Outline each uninfected red blood cell.
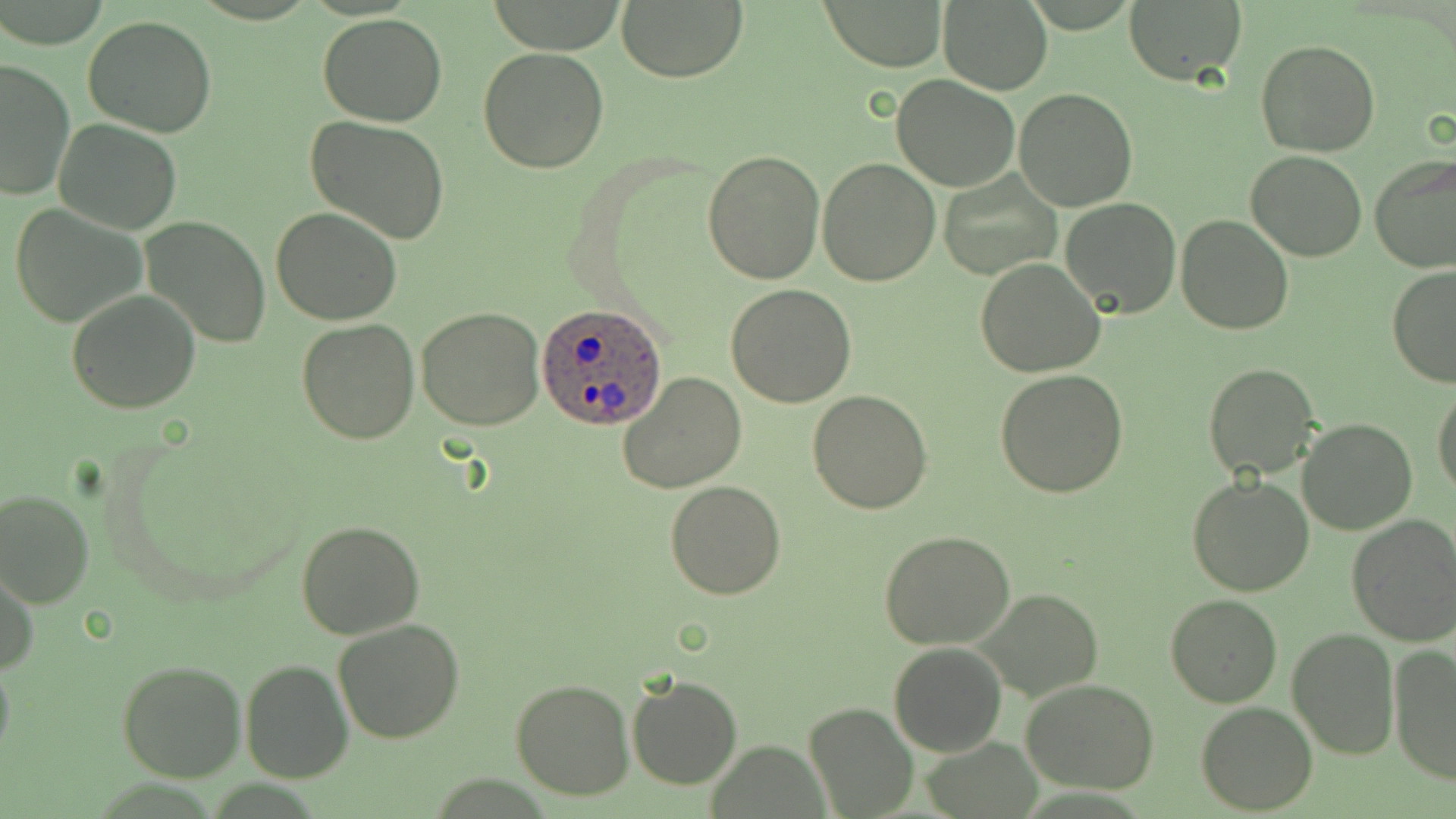
Approximate bounding boxes as (x1,y1)-(x2,y2) corner pairs in pixels.
Uninfected red blood cells: (617,0)-(746,82), (936,0)-(1054,95), (822,1)-(947,71), (1122,1)-(1247,85), (319,13)-(448,126), (82,15)-(219,138), (1255,37)-(1380,155), (477,48)-(609,174), (1,59)-(74,200), (891,74)-(1020,191), (1013,87)-(1140,211), (305,116)-(451,243), (54,120)-(184,235), (701,148)-(825,285), (1245,150)-(1368,260), (1369,153)-(1456,274), (816,157)-(941,287), (940,171)-(1062,278), (1060,198)-(1182,317), (9,203)-(149,330), (271,208)-(404,327), (1175,214)-(1293,334), (140,217)-(271,348), (976,257)-(1107,378), (1387,265)-(1456,387), (726,285)-(859,407), (65,289)-(201,413), (416,306)-(546,430), (296,318)-(419,444), (1204,362)-(1320,481), (994,370)-(1128,498), (618,372)-(748,494), (1432,385)-(1456,498), (806,390)-(933,514), (1298,418)-(1416,534), (1186,475)-(1315,596), (663,481)-(787,600), (0,487)-(95,607), (1345,514)-(1456,647), (295,520)-(425,639), (878,530)-(1014,649), (1,566)-(38,677), (979,588)-(1099,701), (1166,594)-(1282,708), (332,618)-(466,743), (1284,626)-(1399,760), (888,642)-(1007,757), (1388,644)-(1456,782), (0,652)-(15,775), (116,659)-(247,783), (241,659)-(352,783), (626,675)-(743,789), (1021,678)-(1160,795), (511,679)-(634,801), (1195,701)-(1318,816), (804,702)-(918,818).

slide-level diagnosis = Plasmodium ovale
modality = light microscopy
magnification = 1000x
preparation = thin blood smear
stain = May-Grünwald-Giemsa
field of view = one of a larger specimen
Plasmodium ovale-infected red blood cell locations = approximate bounding boxes as (x1,y1)-(x2,y2) corner pairs in pixels: (537,301)-(665,430)
image size = 1456×819 pixels